Outline each blood parasite and name the species.
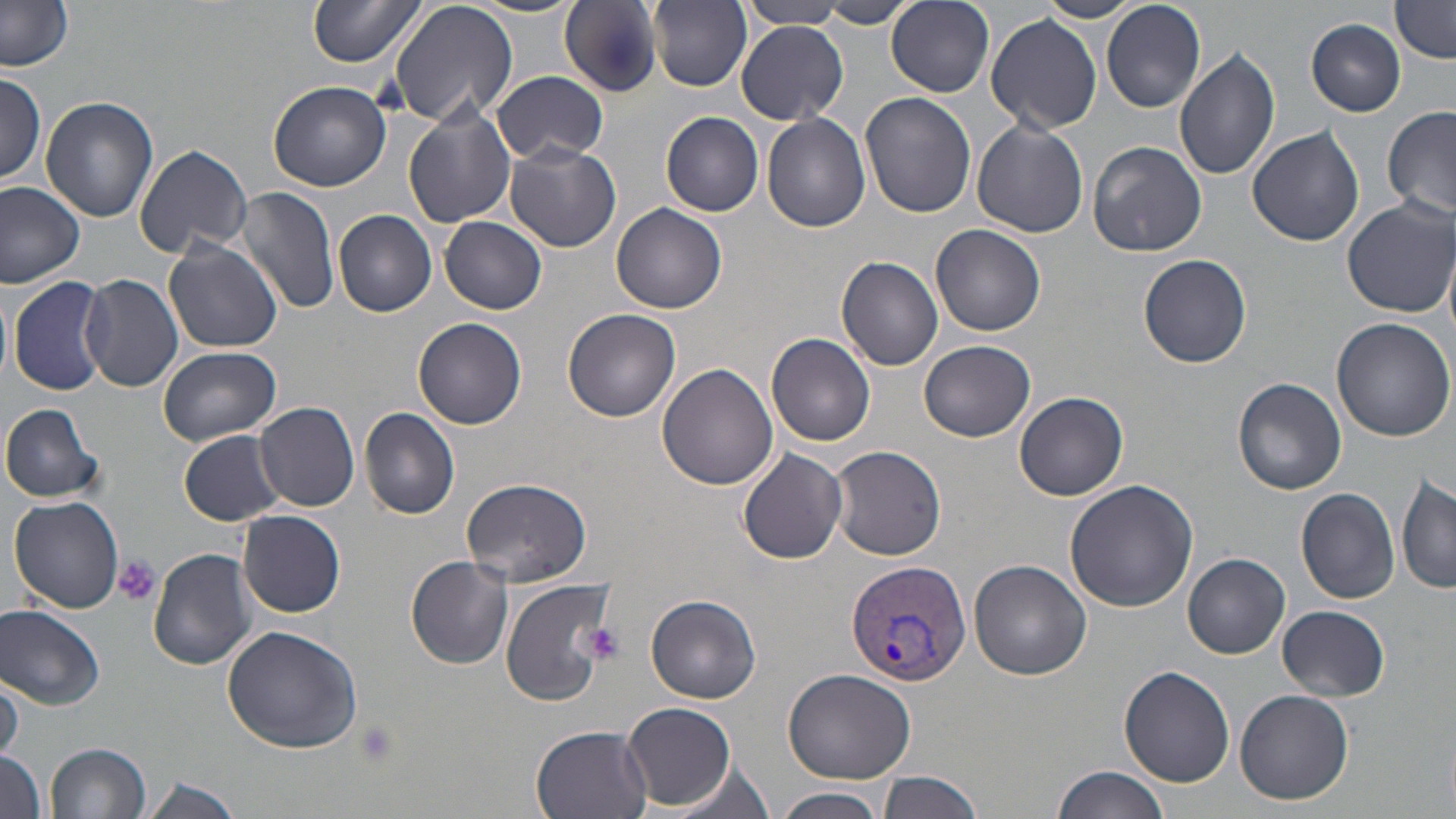
Approximate bounding boxes as (x1, y1, x2, y2) in pixels.
Plasmodium vivax-infected red blood cells: (843, 558, 970, 687).
No Plasmodium falciparum, Plasmodium ovale, Plasmodium malariae, Babesia divergens, or Trypanosoma brucei observed.

slide-level diagnosis = Plasmodium vivax
field of view = single
preparation = thin blood film
magnification = 1000x
modality = optical microscopy
uninfected red blood cell locations = approximate bounding boxes as (x1, y1, x2, y2) in pixels: (307, 0, 428, 68), (390, 0, 518, 128), (1036, 0, 1145, 23), (466, 1, 583, 19), (560, 1, 665, 94), (650, 1, 751, 89), (820, 1, 916, 29), (887, 1, 994, 96), (741, 2, 848, 29), (1102, 2, 1205, 112), (1389, 2, 1455, 63), (0, 3, 74, 71), (986, 12, 1104, 134), (1306, 19, 1407, 116), (735, 23, 849, 126), (1173, 45, 1283, 180), (492, 70, 609, 164), (0, 71, 47, 187), (268, 80, 392, 191), (860, 91, 977, 219), (41, 97, 160, 224), (404, 97, 517, 231), (1380, 106, 1455, 223), (662, 111, 765, 216), (761, 114, 871, 232), (972, 119, 1090, 238), (1247, 125, 1365, 246), (1087, 140, 1206, 257), (504, 143, 620, 252), (133, 145, 253, 259), (0, 180, 85, 289), (236, 186, 340, 316), (1340, 197, 1454, 317), (611, 203, 728, 314), (334, 210, 438, 317), (440, 217, 548, 313), (932, 223, 1046, 335), (162, 239, 283, 353), (1139, 253, 1253, 367), (835, 255, 945, 370), (79, 273, 184, 391), (8, 276, 109, 398), (0, 288, 12, 383), (563, 309, 681, 423), (413, 317, 528, 429), (1330, 317, 1456, 442), (766, 332, 876, 447), (919, 340, 1036, 440), (157, 345, 281, 445), (657, 361, 779, 489), (1231, 377, 1347, 496), (1015, 392, 1128, 500), (255, 401, 360, 512), (0, 402, 104, 504), (360, 407, 460, 520), (178, 430, 286, 525), (829, 445, 947, 560), (738, 446, 848, 567), (1396, 471, 1456, 595), (461, 475, 591, 588), (1065, 480, 1199, 612), (1294, 488, 1401, 604), (8, 496, 124, 614), (236, 509, 347, 618), (149, 548, 258, 669), (1184, 551, 1291, 658), (406, 557, 514, 668), (969, 559, 1091, 679), (500, 576, 617, 709), (645, 594, 762, 703), (0, 602, 106, 712), (1278, 605, 1389, 701), (221, 625, 363, 754), (1118, 665, 1236, 790), (783, 667, 917, 783), (0, 670, 24, 762), (1234, 688, 1356, 805), (623, 703, 736, 808), (527, 723, 655, 818), (46, 741, 151, 819), (1, 749, 47, 819), (668, 759, 776, 819), (1051, 765, 1169, 819), (878, 770, 983, 819), (142, 775, 243, 819), (774, 789, 889, 819)
platelet locations = approximate bounding boxes as (x1, y1, x2, y2) in pixels: (111, 554, 160, 607), (577, 621, 626, 665), (352, 721, 399, 770)
image size = 1456×819 pixels
stain = May-Grünwald-Giemsa